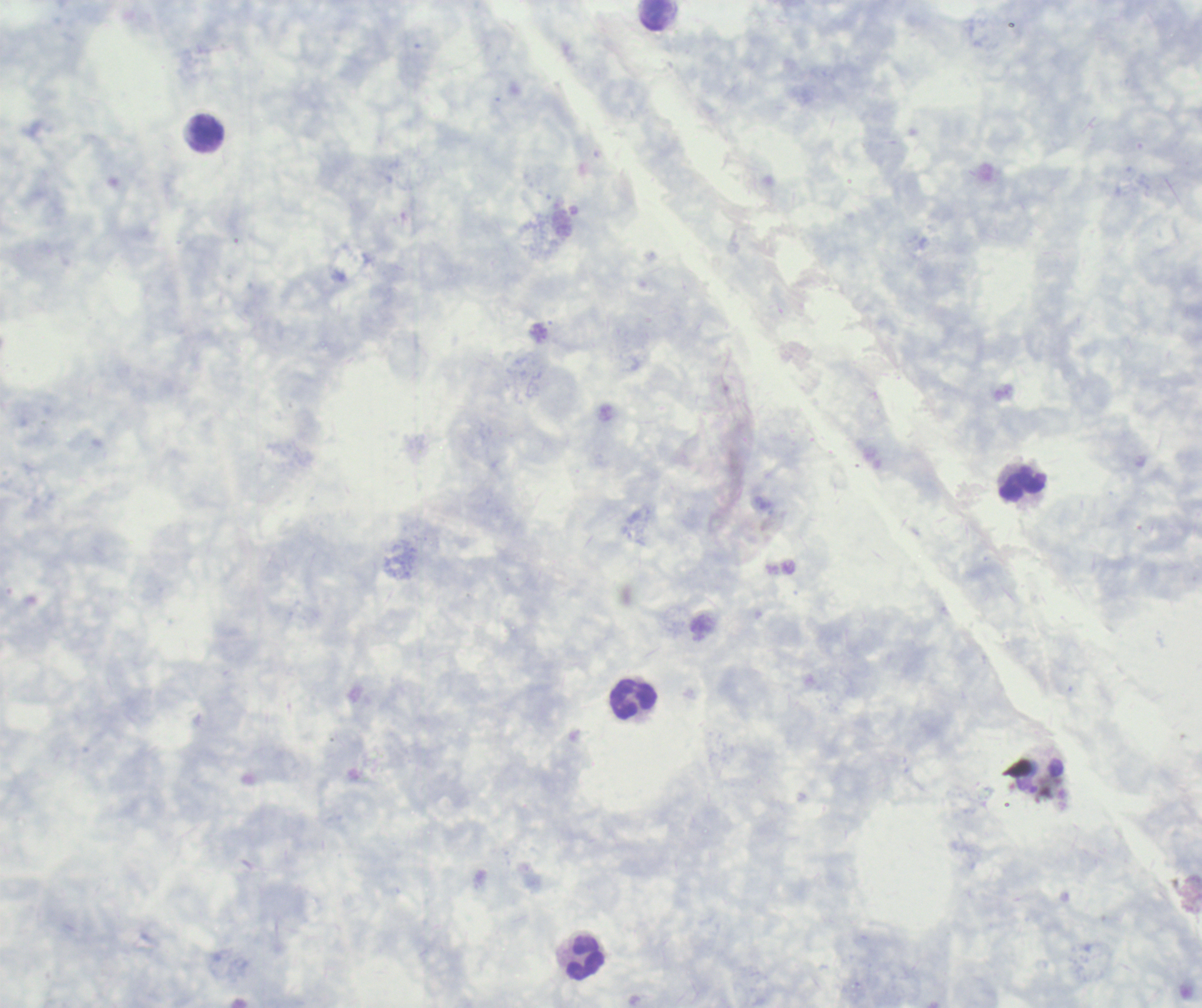 Approximate centers as (x, y) in pixels. Leukocyte locations: (657, 15), (206, 134), (1022, 484), (635, 699), (587, 958). Image is 1202×1008 pixels. Thick blood film. Previously used in an actual diagnosis. Captured at 100x magnification. Coloration quality: good. Romanowsky-stained preparation. Background quality: unsatisfactory. Result: no Plasmodium parasites seen. One field from this slide.